Give the position of every malaria parasite.
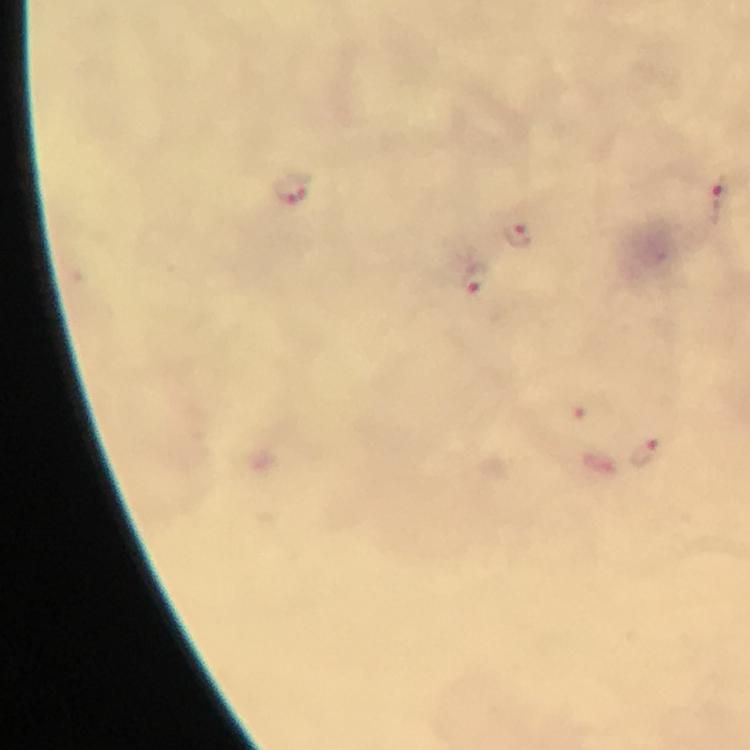
Approximate object centers, in pixels from the top-left corner.
Malaria parasites: (x=291, y=189), (x=722, y=198), (x=517, y=235), (x=474, y=280), (x=644, y=450).

Summary:
  - Stain: Giemsa
  - Context: from a diagnostic examination for malaria
  - Image size: 750×750 pixels
  - Capture: smartphone photograph through a microscope
  - Cropped from: a single field of view
  - Immersion oil: used
  - Preparation: thick blood smear
  - Magnification: 100x